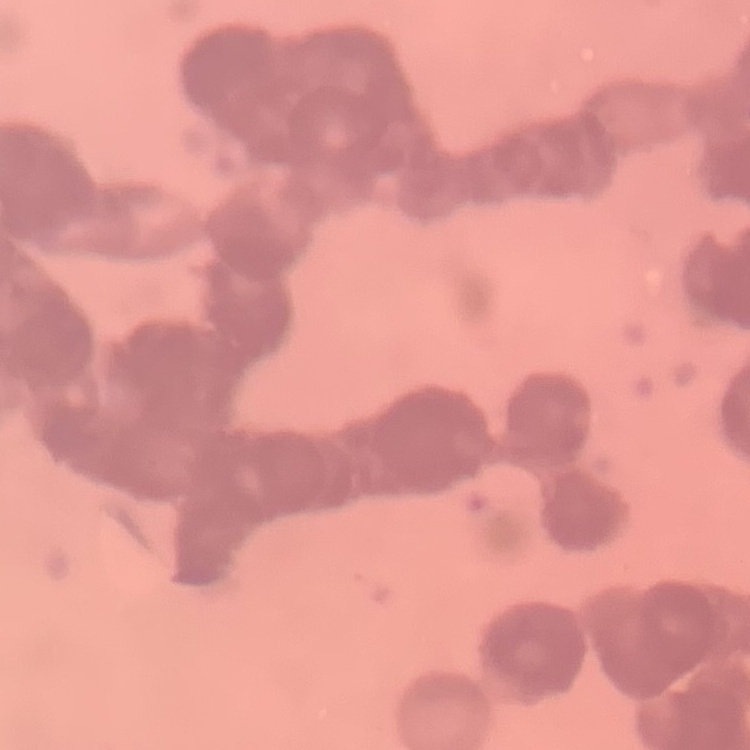
Summary:
  - Erythrocyte morphology: rouleaux formation
  - Image type: square crop of a larger photomicrograph
  - Preparation: thin blood smear
  - Stain: Field's or Giemsa